State which cell type is depicted.
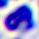
This is a leukocyte.

Photomicrograph. Captured at 400x magnification.